Report the malaria status of this cell.
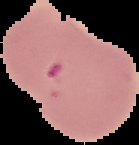

Parasitized.

Image is 139×145 pixels. Cell region segmented out of the field of view; the surrounding area is masked to black. From a thin blood film.